Classify this cell by malaria status.
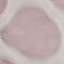
It is uninfected.

{
  "capture": "smartphone camera at the microscope eyepiece",
  "preparation": "thin blood smear",
  "image_type": "automatically extracted cell patch, resized to 64 × 64 pixels",
  "stain": "Giemsa"
}